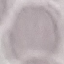

Malaria status: uninfected. Giemsa stain. Photographed with a smartphone camera at the microscope eyepiece. Thin blood film. Cell patch, automatically extracted from a larger field of view and resized to 64 × 64 pixels.